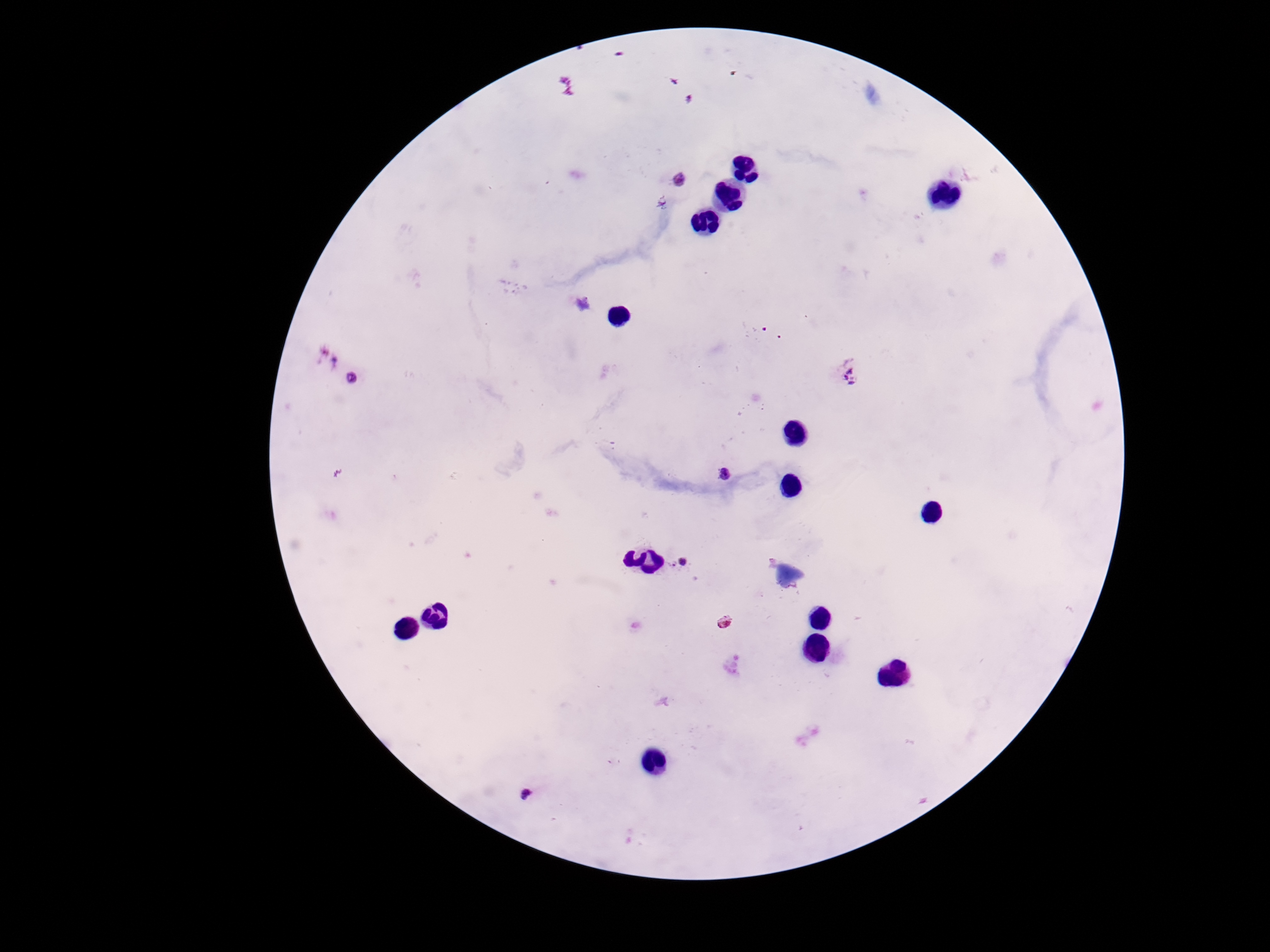
Approximate centers as (x, y) in pixels. Plasmodium parasite locations: (566, 87), (679, 180), (850, 376), (354, 378), (724, 475), (680, 562), (528, 791). Patient malaria status: infected. One field from this slide. Giemsa stain. Photographed through the microscope eyepiece with a smartphone camera. Image is 1270×952 pixels. 100x magnification. Thick peripheral-blood smear.